Outline each Plasmodium falciparum-infected red blood cell.
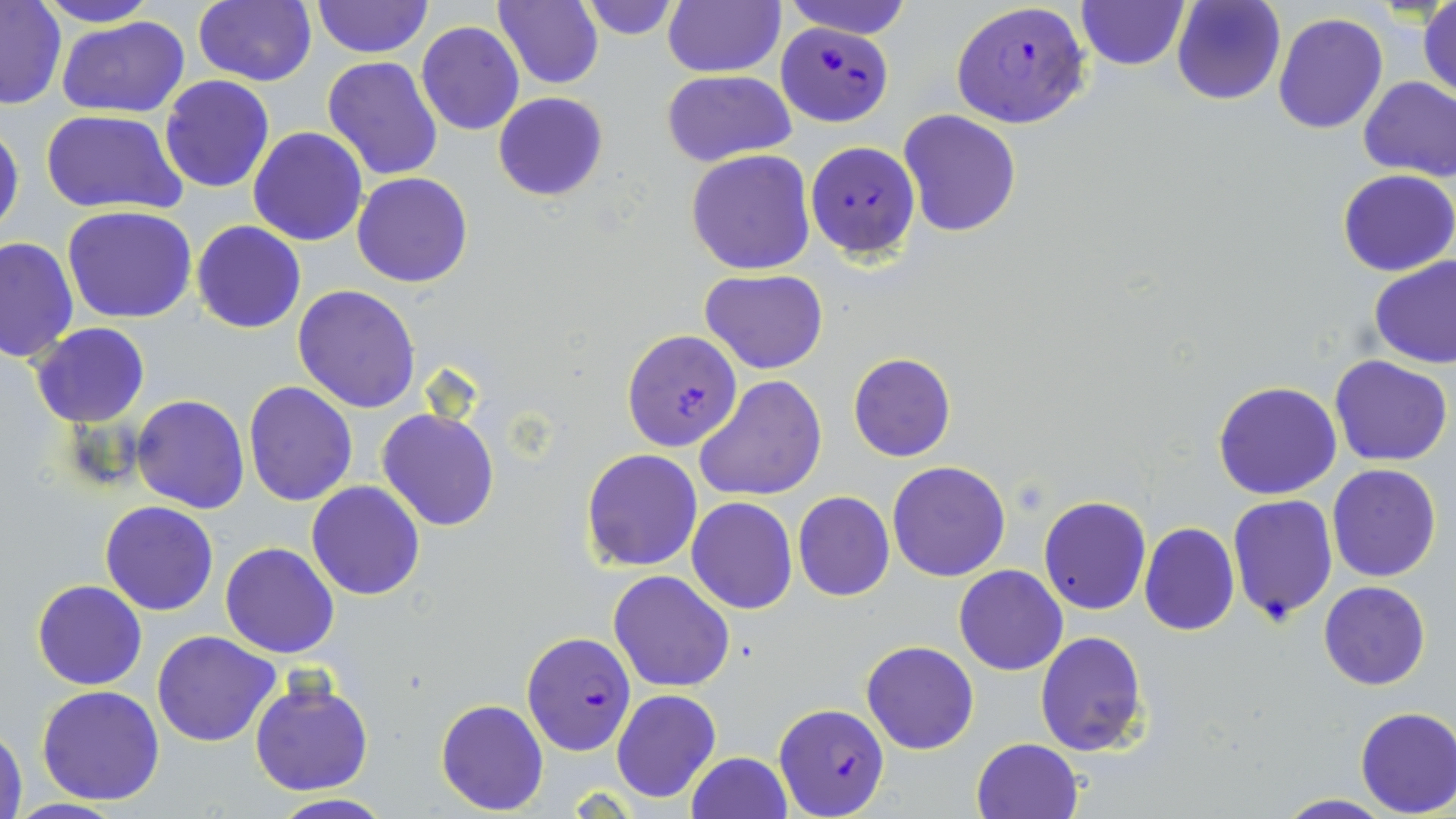
Approximate bounding boxes as named x1/y1/x2/y2 corners in pixels.
Plasmodium falciparum-infected red blood cells: (x1=950, y1=1, x2=1093, y2=130), (x1=773, y1=25, x2=896, y2=127), (x1=806, y1=140, x2=919, y2=261), (x1=622, y1=331, x2=745, y2=451), (x1=520, y1=629, x2=639, y2=758), (x1=775, y1=702, x2=890, y2=818).

Uninfected red blood cell locations: (x1=36, y1=0, x2=158, y2=27), (x1=193, y1=0, x2=316, y2=87), (x1=310, y1=0, x2=434, y2=59), (x1=495, y1=0, x2=604, y2=89), (x1=577, y1=0, x2=682, y2=39), (x1=663, y1=0, x2=785, y2=78), (x1=778, y1=0, x2=914, y2=39), (x1=1171, y1=0, x2=1287, y2=105), (x1=1075, y1=1, x2=1190, y2=72), (x1=1417, y1=1, x2=1455, y2=103), (x1=0, y1=2, x2=66, y2=111), (x1=1273, y1=11, x2=1389, y2=134), (x1=57, y1=16, x2=191, y2=119), (x1=417, y1=22, x2=524, y2=136), (x1=322, y1=56, x2=443, y2=181), (x1=662, y1=70, x2=795, y2=165), (x1=160, y1=75, x2=275, y2=193), (x1=1358, y1=75, x2=1456, y2=182), (x1=494, y1=92, x2=609, y2=201), (x1=41, y1=109, x2=187, y2=216), (x1=897, y1=110, x2=1023, y2=239), (x1=0, y1=119, x2=24, y2=241), (x1=247, y1=126, x2=369, y2=246), (x1=684, y1=149, x2=816, y2=276), (x1=1337, y1=170, x2=1455, y2=275), (x1=352, y1=173, x2=473, y2=288), (x1=62, y1=205, x2=197, y2=323), (x1=191, y1=220, x2=307, y2=334), (x1=1, y1=235, x2=79, y2=364), (x1=1368, y1=254, x2=1456, y2=369), (x1=701, y1=268, x2=828, y2=375), (x1=293, y1=284, x2=422, y2=413), (x1=30, y1=322, x2=150, y2=427), (x1=848, y1=352, x2=955, y2=463), (x1=1330, y1=355, x2=1453, y2=466), (x1=694, y1=375, x2=825, y2=501), (x1=243, y1=380, x2=358, y2=505), (x1=1212, y1=381, x2=1342, y2=501), (x1=131, y1=394, x2=250, y2=513), (x1=378, y1=407, x2=499, y2=532), (x1=580, y1=447, x2=704, y2=571), (x1=886, y1=461, x2=1012, y2=582), (x1=1327, y1=463, x2=1442, y2=582), (x1=307, y1=481, x2=425, y2=600), (x1=793, y1=491, x2=895, y2=602), (x1=686, y1=496, x2=797, y2=614), (x1=1038, y1=496, x2=1151, y2=615), (x1=1226, y1=496, x2=1338, y2=624), (x1=99, y1=501, x2=220, y2=617), (x1=1139, y1=522, x2=1239, y2=637), (x1=220, y1=541, x2=340, y2=659), (x1=953, y1=565, x2=1068, y2=676), (x1=608, y1=569, x2=735, y2=692), (x1=32, y1=579, x2=147, y2=690), (x1=1318, y1=581, x2=1431, y2=690), (x1=151, y1=630, x2=281, y2=747), (x1=1034, y1=630, x2=1149, y2=757), (x1=861, y1=639, x2=979, y2=754), (x1=249, y1=676, x2=374, y2=796), (x1=37, y1=684, x2=167, y2=805), (x1=612, y1=689, x2=720, y2=802), (x1=435, y1=698, x2=549, y2=816), (x1=1354, y1=706, x2=1456, y2=817), (x1=1, y1=721, x2=27, y2=818), (x1=971, y1=737, x2=1085, y2=819), (x1=685, y1=751, x2=793, y2=819), (x1=264, y1=794, x2=397, y2=818), (x1=1273, y1=794, x2=1394, y2=819), (x1=7, y1=799, x2=125, y2=818). Slide-level diagnosis: Plasmodium falciparum. One field of a larger specimen. Light microscopy. 1000x magnification. May-Grünwald-Giemsa stain. Thin blood smear. Image is 1456×819 pixels.